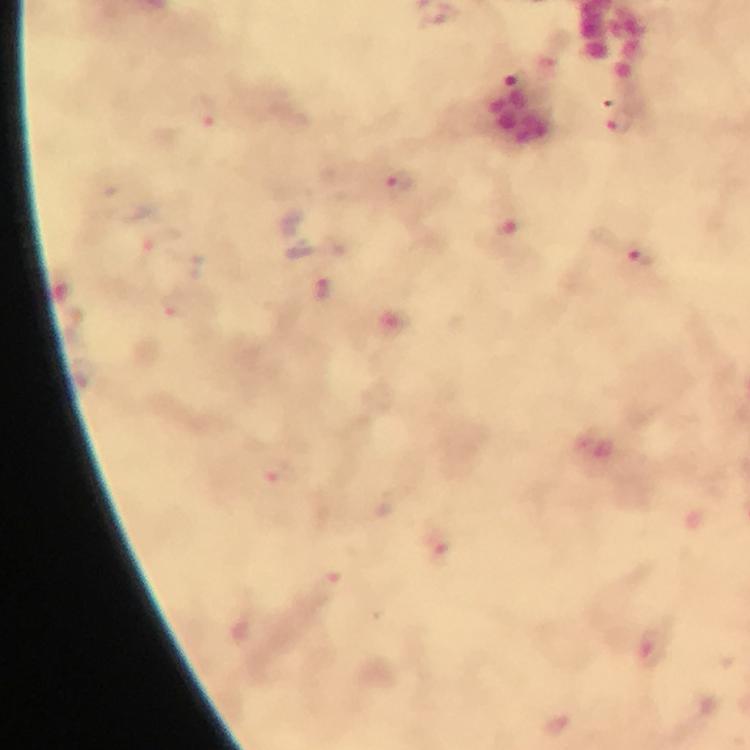
Approximate centers as [x, y] in pixels.
Summary:
  - Plasmodium parasite locations: [513, 84], [209, 112], [621, 122], [399, 183], [510, 233], [158, 241], [638, 259], [324, 288], [176, 303], [440, 548], [652, 648]
  - Context: from a diagnostic examination for malaria
  - Immersion oil: applied
  - Cropped from: one field of view
  - Magnification: 100x
  - Image size: 750×750 pixels
  - Preparation: thick blood film
  - Stain: Giemsa
  - Capture: smartphone mounted on the microscope